Assess this cell for malaria.
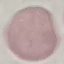
It is uninfected.

Summary:
  - Preparation: thin blood smear
  - Stain: Giemsa
  - Capture: smartphone camera at the microscope eyepiece
  - Image type: cell patch, automatically extracted from a larger field of view and resized to 64 × 64 pixels